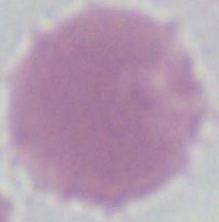

Summary:
  - Identification: erythrocyte
  - Modality: micrograph
  - Magnification: 1000x